Locate and identify every blood parasite.
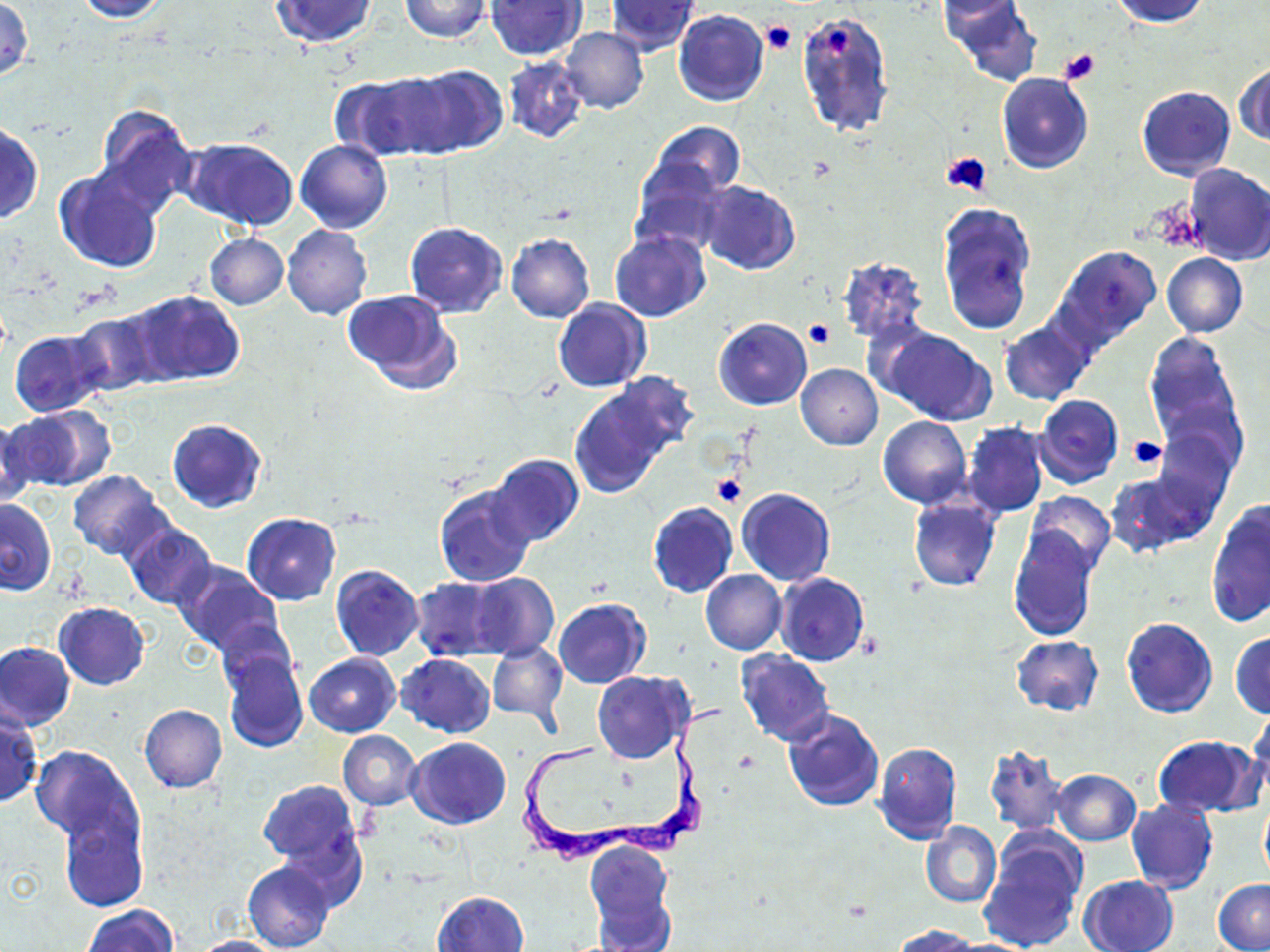
Approximate bounding boxes as (x1, y1, x2, y2) in pixels.
Trypanosoma brucei: (522, 698, 728, 868).
No Plasmodium falciparum, Plasmodium ovale, Plasmodium malariae, Plasmodium vivax, or Babesia divergens observed.

Summary:
  - Platelet locations: (761, 20, 797, 55), (1059, 48, 1100, 84), (941, 150, 993, 197), (803, 319, 834, 348), (1128, 436, 1168, 468), (710, 473, 745, 508)
  - Uninfected red blood cell locations: (72, 0, 169, 21), (269, 0, 377, 48), (399, 0, 490, 42), (1109, 0, 1208, 26), (1, 1, 32, 82), (485, 1, 585, 60), (606, 1, 700, 56), (936, 2, 1024, 26), (946, 5, 1037, 86), (796, 9, 895, 137), (673, 10, 769, 107), (560, 26, 649, 113), (501, 56, 590, 144), (1235, 62, 1270, 146), (403, 63, 507, 156), (329, 73, 437, 161), (996, 73, 1092, 174), (1137, 86, 1235, 180), (92, 105, 198, 216), (647, 120, 745, 201), (0, 122, 43, 224), (184, 138, 300, 231), (295, 138, 392, 234), (1181, 162, 1270, 265), (631, 164, 731, 256), (55, 168, 162, 273), (699, 180, 800, 275), (937, 201, 1038, 336), (404, 222, 508, 317), (282, 225, 372, 320), (610, 230, 711, 322), (205, 233, 289, 309), (506, 233, 595, 324), (1053, 244, 1163, 352), (1161, 253, 1247, 337), (837, 257, 929, 345), (344, 288, 463, 393), (128, 291, 246, 385), (553, 298, 650, 392), (69, 312, 161, 398), (714, 317, 812, 410), (999, 320, 1093, 406), (878, 327, 997, 426), (9, 330, 107, 417), (1143, 333, 1244, 464), (796, 364, 883, 450), (571, 380, 685, 495), (1035, 395, 1123, 487), (7, 407, 112, 493), (0, 416, 34, 505), (878, 417, 971, 509), (167, 418, 267, 512), (962, 423, 1049, 517), (1153, 427, 1236, 518), (489, 453, 584, 547), (68, 469, 168, 560), (1105, 469, 1213, 556), (433, 483, 537, 586), (737, 487, 835, 586), (1024, 491, 1116, 578), (908, 498, 1001, 591), (0, 499, 56, 595), (1206, 500, 1270, 629), (647, 501, 738, 598), (243, 513, 340, 604), (122, 522, 216, 610), (1007, 529, 1097, 639), (174, 561, 285, 658), (330, 564, 423, 660), (700, 569, 786, 654), (467, 572, 558, 661), (774, 572, 869, 666), (411, 576, 505, 661), (553, 598, 650, 689), (54, 603, 150, 689), (1121, 618, 1218, 719), (216, 620, 298, 694), (1230, 631, 1270, 718), (1011, 635, 1104, 715), (486, 639, 567, 724), (0, 643, 75, 730), (220, 649, 308, 755), (736, 650, 834, 745), (305, 653, 400, 737), (397, 653, 495, 737), (593, 671, 692, 764), (139, 704, 227, 792), (783, 707, 884, 810), (0, 708, 41, 807), (1247, 712, 1270, 808), (338, 730, 421, 810), (1152, 734, 1264, 818), (406, 738, 509, 829), (873, 741, 962, 845), (30, 746, 141, 848), (984, 746, 1069, 835), (1052, 769, 1140, 846), (257, 779, 363, 873), (1259, 796, 1270, 885), (1124, 798, 1218, 895), (56, 804, 148, 914), (921, 821, 1001, 908), (978, 836, 1085, 952), (583, 841, 675, 948), (242, 859, 335, 952), (1077, 874, 1179, 952), (1214, 879, 1270, 952), (433, 890, 530, 952), (82, 905, 177, 952), (894, 924, 976, 952), (188, 935, 284, 951)
  - Slide-level diagnosis: Trypanosoma brucei
  - Preparation: thin blood smear
  - Image size: 1270×952 pixels
  - Magnification: 1000x
  - Modality: light microscopy
  - Field of view: single
  - Stain: May-Grünwald-Giemsa